State which parasite is depicted.
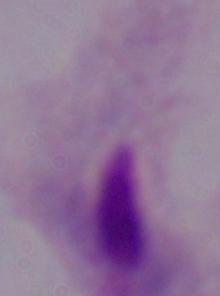
A trichomonad.

Summary:
  - Magnification: 1000x
  - Modality: micrograph